State the blood parasite species.
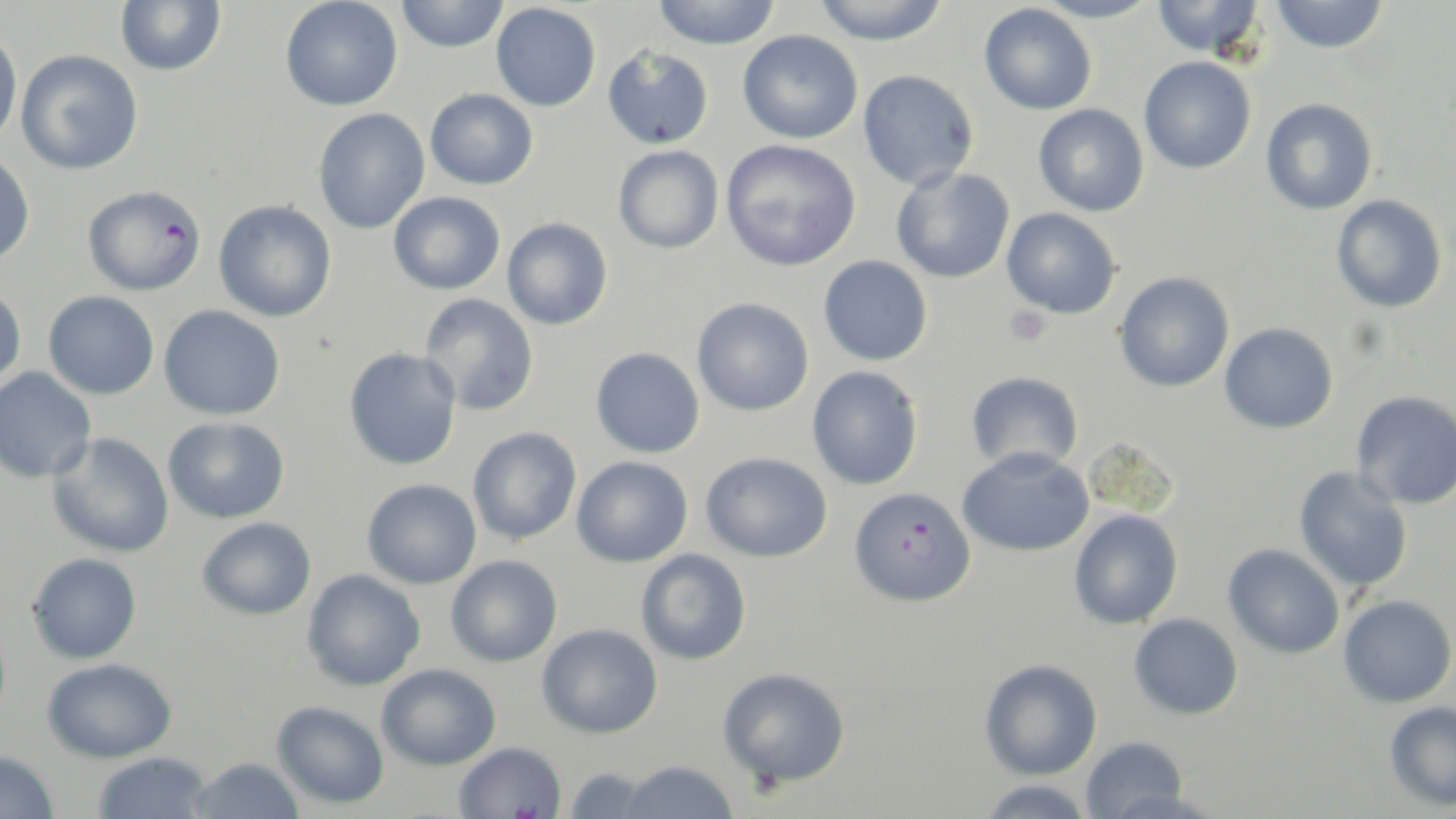
Plasmodium falciparum.

field_of_view: one of a larger specimen
plasmodium_falciparum_infected_red_blood_cell_locations: 'approximate bounding boxes as [x1, y1, x2, y2] in pixels: [81, 184, 206, 296], [849, 486, 976, 608]'
uninfected_red_blood_cell_locations: 'approximate bounding boxes as [x1, y1, x2, y2] in pixels: [115, 0, 227, 76], [279, 0, 403, 112], [395, 0, 510, 53], [651, 0, 783, 50], [810, 0, 951, 46], [1033, 0, 1161, 25], [1151, 0, 1266, 59], [1270, 0, 1390, 54], [491, 3, 601, 111], [978, 3, 1097, 115], [0, 25, 22, 149], [737, 30, 863, 144], [603, 45, 714, 150], [16, 49, 144, 175], [1138, 56, 1256, 174], [857, 70, 979, 190], [425, 88, 538, 190], [1260, 98, 1378, 216], [1033, 103, 1149, 216], [312, 108, 430, 234], [720, 138, 861, 272], [613, 145, 724, 254], [0, 150, 36, 267], [891, 167, 1015, 284], [388, 191, 505, 295], [1332, 194, 1447, 313], [213, 200, 338, 322], [1002, 207, 1122, 319], [502, 218, 613, 331], [818, 255, 933, 366], [1114, 271, 1235, 392], [0, 283, 27, 389], [43, 290, 159, 400], [419, 293, 539, 416], [692, 298, 814, 416], [158, 304, 285, 421], [1219, 322, 1339, 434], [590, 346, 705, 458], [343, 347, 462, 471], [807, 366, 924, 490], [0, 367, 97, 484], [966, 371, 1084, 473], [1351, 390, 1456, 509], [163, 416, 290, 524], [467, 426, 582, 544], [47, 432, 175, 558], [1081, 436, 1181, 520], [956, 447, 1094, 557], [700, 451, 833, 562], [571, 455, 693, 567], [1293, 466, 1413, 592], [362, 479, 482, 589], [1068, 508, 1184, 629], [197, 517, 317, 620], [1223, 543, 1345, 659], [635, 548, 752, 665], [27, 552, 142, 664], [445, 554, 563, 667], [301, 568, 426, 691], [1338, 594, 1456, 707], [1128, 613, 1244, 720], [537, 623, 662, 739], [41, 657, 178, 763], [979, 658, 1102, 780], [377, 663, 501, 770], [717, 666, 851, 788], [271, 700, 390, 809], [1384, 701, 1456, 811], [1080, 736, 1191, 818], [453, 741, 567, 818], [0, 749, 60, 819], [92, 751, 214, 818], [188, 757, 306, 818], [617, 759, 740, 818], [562, 766, 657, 818], [976, 778, 1097, 818]'
platelet_locations: 'approximate bounding boxes as [x1, y1, x2, y2] in pixels: [1003, 305, 1053, 347]'
modality: light microscopy
image_size: 1456×819 pixels
preparation: thin blood film
stain: May-Grünwald-Giemsa
magnification: 1000x